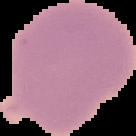

result = no malaria parasites detected
image size = 136×136 pixels
image type = segmented cell region on a black background
preparation = thin blood smear